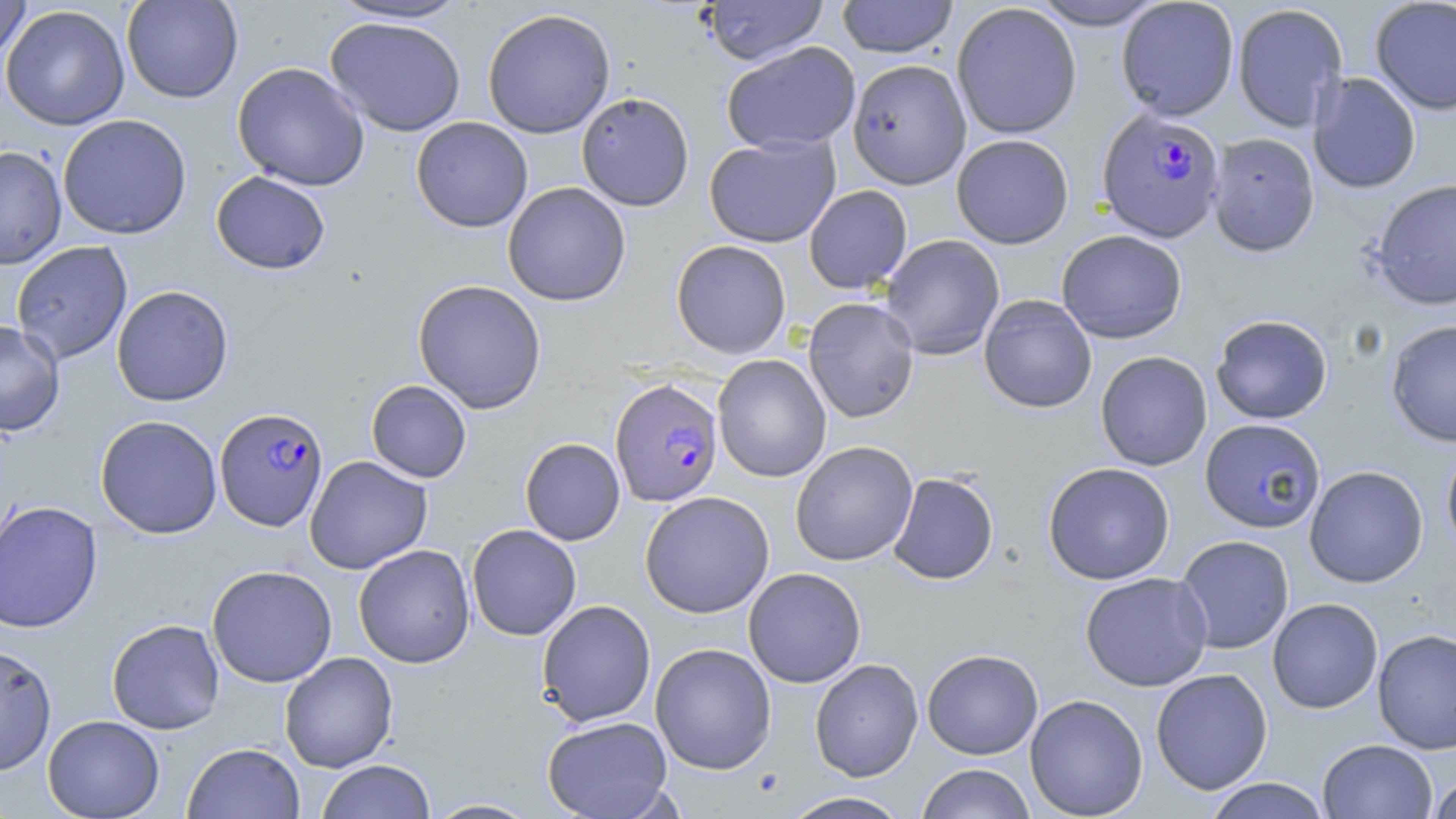

slide_level_diagnosis: Plasmodium falciparum
image_size: 1456×819 pixels
stain: May-Grünwald-Giemsa
modality: light microscopy
uninfected_red_blood_cell_locations: 'approximate bounding boxes as [x1, y1, x2, y2] in pixels: [0, 0, 32, 62], [122, 0, 243, 103], [836, 0, 959, 58], [1027, 0, 1169, 30], [1116, 0, 1239, 121], [1370, 0, 1456, 115], [325, 1, 475, 24], [702, 1, 829, 65], [951, 3, 1082, 139], [1232, 3, 1348, 133], [1, 4, 130, 130], [481, 8, 616, 139], [324, 16, 467, 137], [721, 41, 861, 154], [847, 59, 972, 189], [231, 62, 371, 191], [1308, 72, 1421, 194], [576, 92, 694, 211], [58, 113, 192, 240], [411, 117, 533, 233], [1208, 132, 1320, 256], [951, 134, 1074, 249], [704, 135, 841, 248], [0, 146, 67, 269], [211, 171, 330, 274], [1370, 179, 1456, 310], [502, 182, 631, 306], [804, 185, 912, 294], [1056, 229, 1188, 344], [880, 234, 1005, 360], [671, 240, 792, 359], [11, 241, 132, 365], [412, 279, 547, 414], [111, 285, 234, 406], [978, 294, 1097, 413], [803, 297, 920, 423], [1210, 314, 1333, 424], [1385, 319, 1456, 447], [0, 320, 65, 436], [1095, 351, 1212, 471], [713, 355, 831, 482], [366, 380, 472, 483], [95, 415, 222, 539], [1200, 418, 1326, 533], [520, 438, 625, 545], [790, 441, 918, 566], [1441, 442, 1456, 559], [304, 455, 433, 574], [1043, 462, 1175, 585], [1304, 465, 1429, 588], [887, 472, 999, 585], [640, 491, 774, 618], [0, 500, 104, 633], [466, 524, 582, 641], [1175, 535, 1294, 654], [353, 544, 475, 669], [206, 565, 337, 687], [743, 567, 866, 688], [1080, 571, 1212, 691], [1267, 598, 1383, 714], [536, 599, 656, 727], [106, 618, 225, 734], [1372, 629, 1456, 755], [0, 643, 57, 776], [650, 643, 777, 774], [922, 648, 1043, 759], [279, 651, 398, 773], [809, 658, 923, 782], [1151, 668, 1273, 795], [1025, 694, 1148, 819], [42, 715, 164, 819], [542, 715, 674, 819], [1317, 739, 1437, 818], [182, 742, 305, 818], [316, 760, 436, 819], [915, 763, 1037, 819], [1427, 772, 1456, 818], [1202, 778, 1332, 818], [779, 791, 913, 819], [423, 798, 542, 818]'
magnification: 1000x
field_of_view: one of a larger specimen
plasmodium_falciparum_infected_red_blood_cell_locations: 'approximate bounding boxes as [x1, y1, x2, y2] in pixels: [1097, 108, 1226, 243], [609, 377, 722, 507], [214, 407, 329, 531]'
preparation: thin blood film